Report the malaria status of this cell.
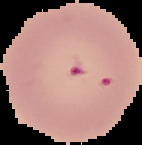
Parasitized.

Image is 142×145 pixels. Cell region segmented out of the field of view; the surrounding area is masked to black. From a thin blood smear.